Point out each Plasmodium parasite.
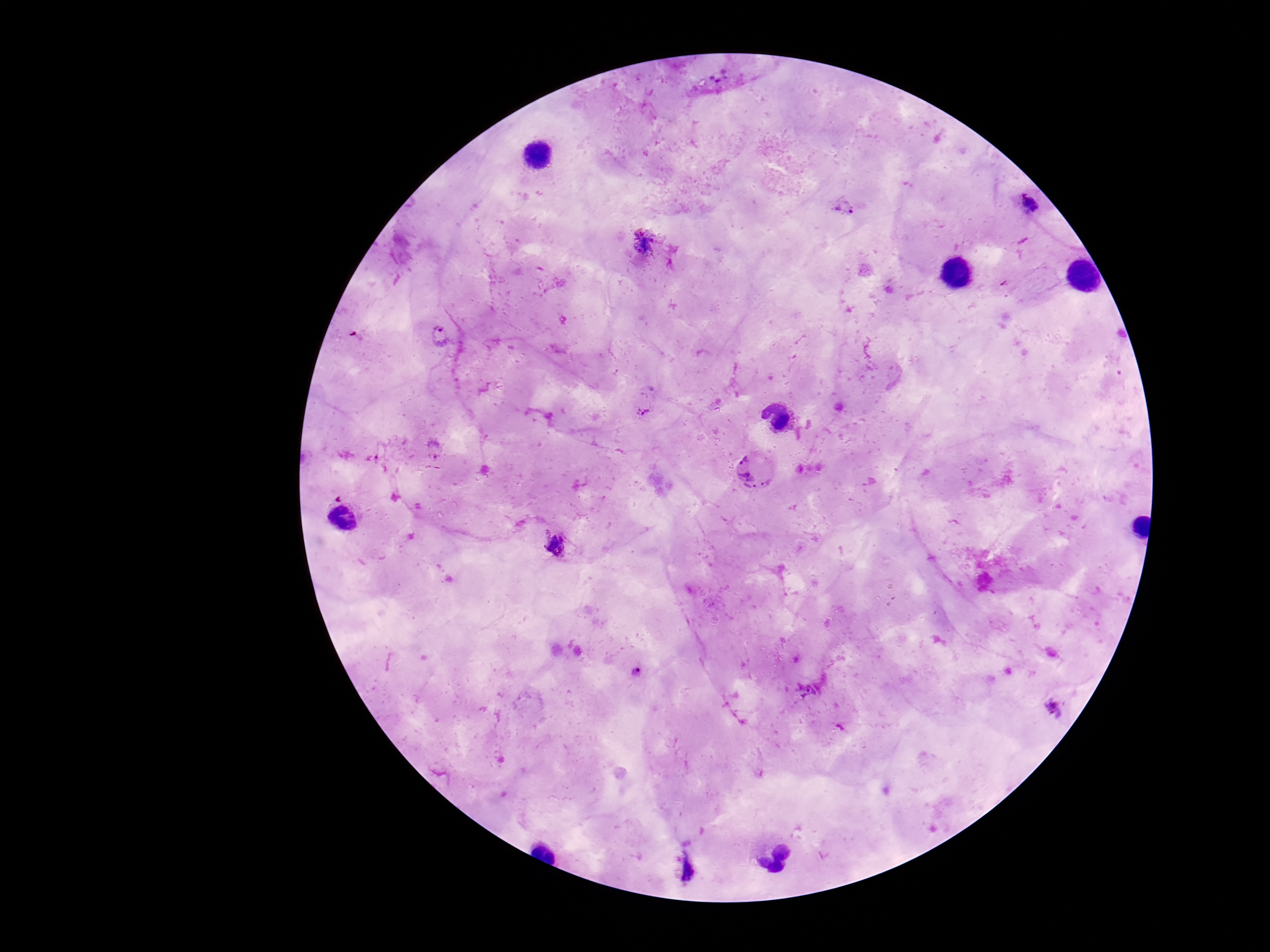
Approximate centers as {x, y} in pixels.
Plasmodium parasites: {717, 75}, {1029, 204}, {845, 206}, {645, 242}, {440, 335}, {647, 401}, {435, 450}, {754, 468}, {557, 546}, {806, 691}, {1054, 708}, {687, 868}.

Single field of view. Thick blood smear. Giemsa-stained preparation. Image is 1270×952 pixels. 100x magnification. Smartphone photograph taken through the microscope eyepiece. Patient malaria status: infected.